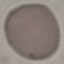
{
  "result": "no malaria parasites detected",
  "capture": "smartphone through the microscope eyepiece",
  "stain": "Giemsa",
  "preparation": "thin blood film",
  "image_type": "automatically extracted cell patch, resized to 64 × 64 pixels"
}